Identify the blood parasite species.
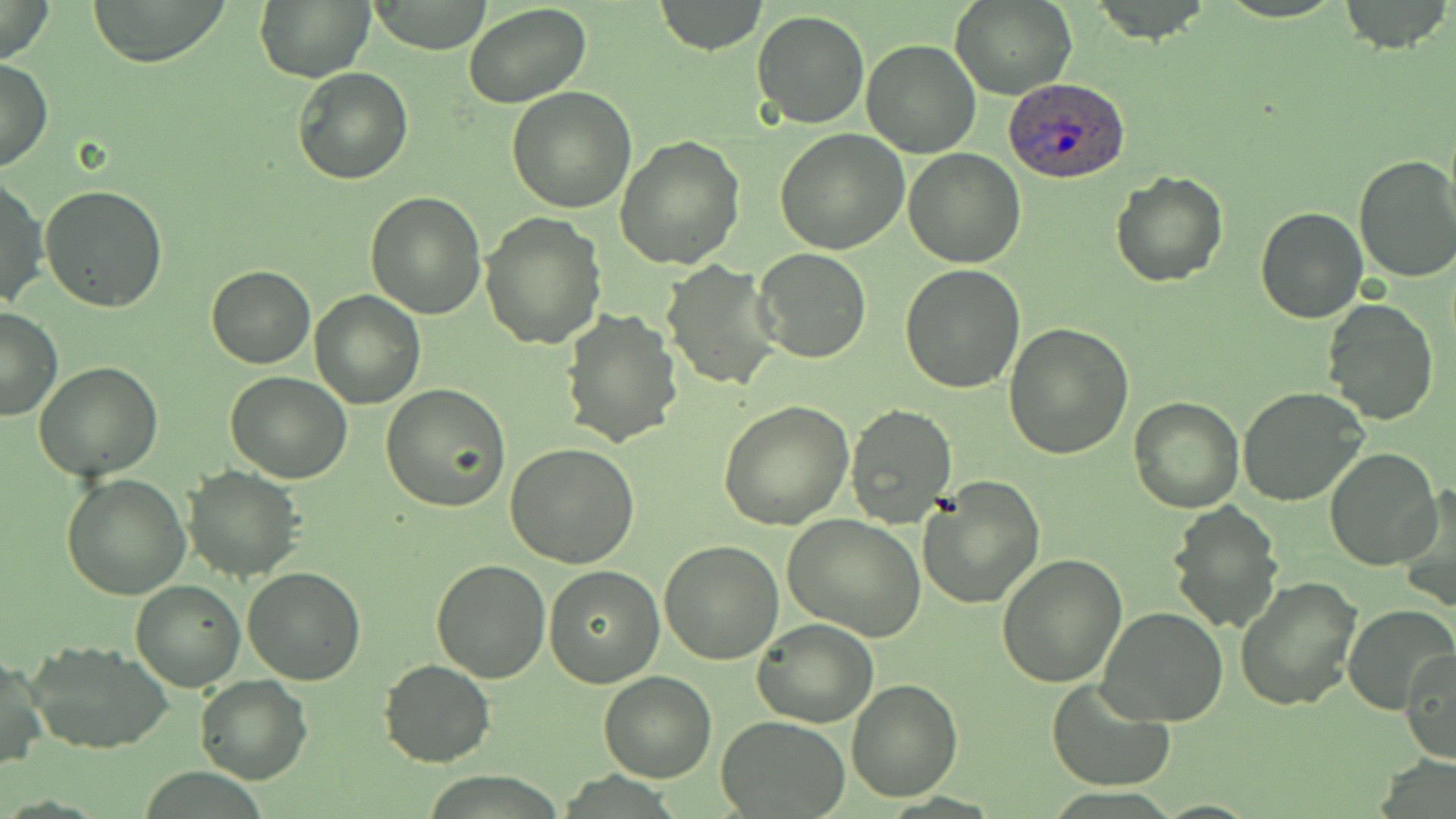
Plasmodium ovale.

stain = May-Grünwald-Giemsa
magnification = 1000x
Plasmodium ovale-infected red blood cell locations = approximate bounding boxes as named x1/y1/x2/y2 corners in pixels: (x1=1004, y1=77, x2=1129, y2=183)
field of view = single
preparation = thin blood film
uninfected red blood cell locations = approximate bounding boxes as named x1/y1/x2/y2 corners in pixels: (x1=0, y1=0, x2=54, y2=63), (x1=88, y1=0, x2=229, y2=67), (x1=651, y1=0, x2=769, y2=54), (x1=950, y1=1, x2=1078, y2=100), (x1=1087, y1=1, x2=1215, y2=45), (x1=255, y1=2, x2=373, y2=82), (x1=366, y1=2, x2=490, y2=54), (x1=1337, y1=2, x2=1453, y2=53), (x1=464, y1=3, x2=591, y2=109), (x1=752, y1=11, x2=870, y2=128), (x1=860, y1=37, x2=981, y2=156), (x1=0, y1=56, x2=52, y2=174), (x1=292, y1=66, x2=413, y2=186), (x1=506, y1=86, x2=636, y2=213), (x1=775, y1=128, x2=910, y2=255), (x1=614, y1=134, x2=747, y2=269), (x1=904, y1=147, x2=1025, y2=269), (x1=1353, y1=153, x2=1456, y2=284), (x1=1110, y1=172, x2=1228, y2=289), (x1=0, y1=175, x2=49, y2=309), (x1=40, y1=186, x2=168, y2=313), (x1=365, y1=190, x2=487, y2=319), (x1=1255, y1=206, x2=1367, y2=323), (x1=479, y1=211, x2=607, y2=351), (x1=754, y1=248, x2=873, y2=364), (x1=661, y1=259, x2=783, y2=393), (x1=206, y1=264, x2=314, y2=367), (x1=900, y1=264, x2=1026, y2=393), (x1=311, y1=291, x2=424, y2=408), (x1=1321, y1=297, x2=1438, y2=427), (x1=0, y1=306, x2=62, y2=423), (x1=560, y1=308, x2=684, y2=449), (x1=1004, y1=320, x2=1133, y2=460), (x1=33, y1=362, x2=164, y2=481), (x1=225, y1=371, x2=352, y2=483), (x1=381, y1=384, x2=512, y2=514), (x1=1238, y1=386, x2=1371, y2=509), (x1=1128, y1=396, x2=1245, y2=513), (x1=718, y1=400, x2=853, y2=531), (x1=844, y1=404, x2=958, y2=531), (x1=506, y1=444, x2=640, y2=568), (x1=1324, y1=448, x2=1441, y2=570), (x1=184, y1=466, x2=305, y2=583), (x1=62, y1=473, x2=190, y2=600), (x1=915, y1=475, x2=1045, y2=609), (x1=1394, y1=485, x2=1456, y2=611), (x1=1167, y1=501, x2=1283, y2=633), (x1=782, y1=513, x2=927, y2=641), (x1=659, y1=541, x2=785, y2=664), (x1=997, y1=554, x2=1129, y2=687), (x1=430, y1=559, x2=552, y2=682), (x1=242, y1=565, x2=366, y2=685), (x1=543, y1=565, x2=664, y2=687), (x1=1234, y1=576, x2=1361, y2=710), (x1=131, y1=579, x2=244, y2=692), (x1=1342, y1=604, x2=1456, y2=714), (x1=1096, y1=605, x2=1229, y2=729), (x1=753, y1=617, x2=876, y2=728), (x1=25, y1=640, x2=172, y2=754), (x1=1401, y1=647, x2=1455, y2=765), (x1=0, y1=652, x2=47, y2=774), (x1=378, y1=659, x2=494, y2=768), (x1=598, y1=672, x2=717, y2=782), (x1=195, y1=675, x2=312, y2=784), (x1=1045, y1=677, x2=1176, y2=792), (x1=846, y1=679, x2=962, y2=803), (x1=718, y1=715, x2=850, y2=818)
image size = 1456×819 pixels
modality = optical microscopy